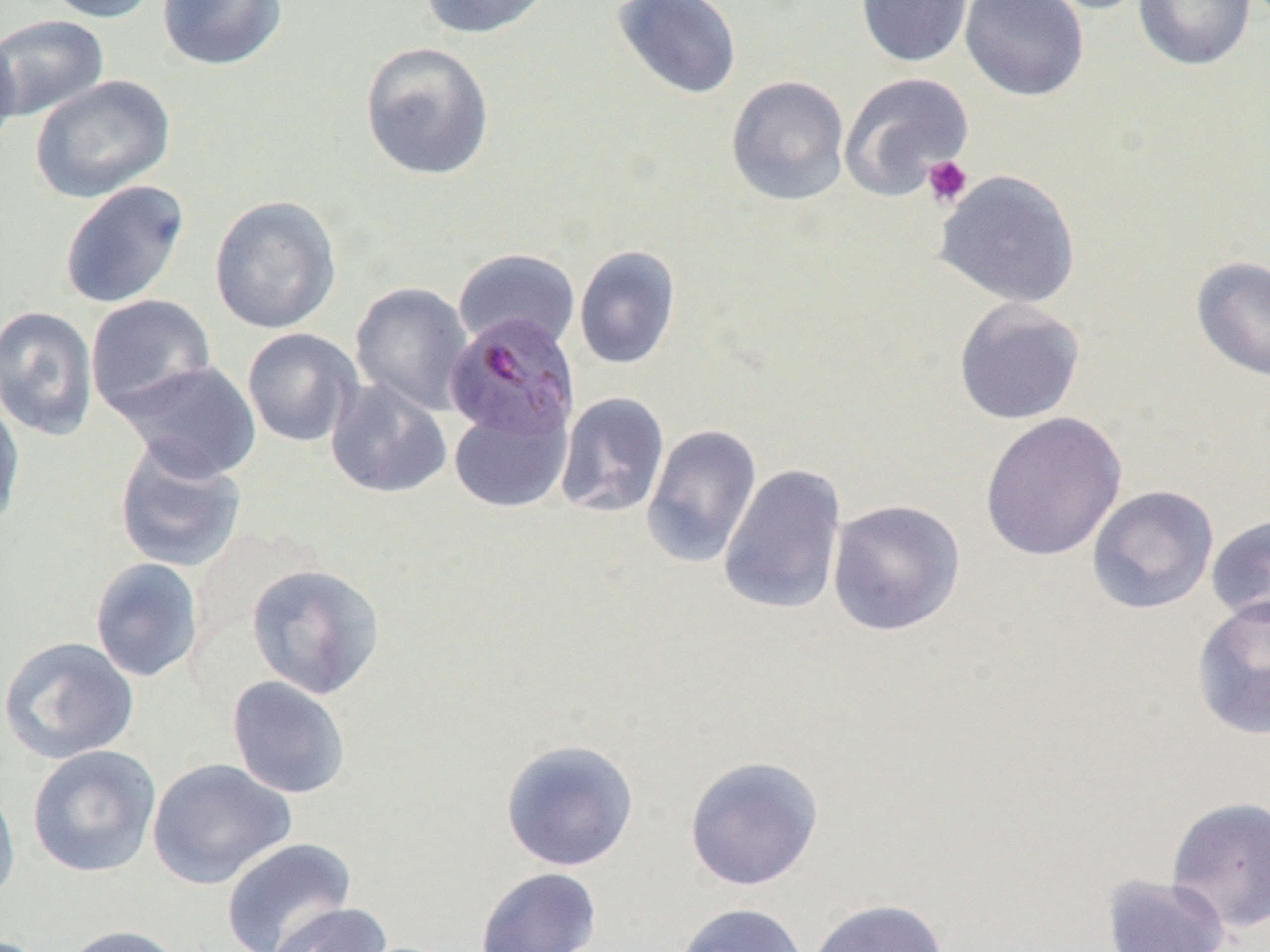

slide_level_diagnosis: Plasmodium malariae
platelet_locations: 'approximate bounding boxes as (x1,y1)-(x2,y2) corner pairs in pixels: (922,155)-(973,208)'
uninfected_red_blood_cell_locations: 'approximate bounding boxes as (x1,y1)-(x2,y2) corner pairs in pixels: (40,0)-(161,23), (157,0)-(288,71), (419,0)-(555,39), (610,0)-(742,100), (856,0)-(972,68), (959,0)-(1089,102), (1031,0)-(1152,14), (1133,0)-(1256,72), (0,15)-(109,122), (0,26)-(22,158), (359,41)-(496,182), (839,72)-(975,199), (30,75)-(175,204), (726,75)-(851,207), (934,169)-(1082,309), (59,180)-(190,310), (209,195)-(342,335), (574,245)-(681,370), (453,248)-(581,352), (1191,257)-(1270,382), (350,282)-(473,415), (85,294)-(217,418), (953,298)-(1086,425), (0,305)-(99,441), (241,328)-(362,447), (116,360)-(261,482), (325,378)-(452,499), (556,392)-(670,518), (0,395)-(26,533), (449,403)-(572,513), (980,411)-(1127,561), (641,423)-(762,568), (114,440)-(247,574), (718,464)-(848,616), (1087,485)-(1219,614), (826,498)-(966,637), (1205,515)-(1270,626), (89,557)-(205,683), (245,563)-(386,700), (1191,596)-(1270,740), (0,636)-(139,764), (226,676)-(352,799), (500,738)-(640,872), (27,745)-(161,878), (684,755)-(824,891), (147,758)-(296,890), (0,778)-(21,910), (1166,796)-(1270,933), (221,837)-(358,952), (475,867)-(602,952), (1101,873)-(1230,952), (806,899)-(948,952), (266,901)-(394,952), (674,902)-(809,952), (59,924)-(186,952)'
preparation: thin blood smear
plasmodium_malariae_infected_red_blood_cell_locations: 'approximate bounding boxes as (x1,y1)-(x2,y2) corner pairs in pixels: (444,314)-(580,442)'
field_of_view: single
magnification: 1000x
modality: light microscopy
image_size: 1270×952 pixels